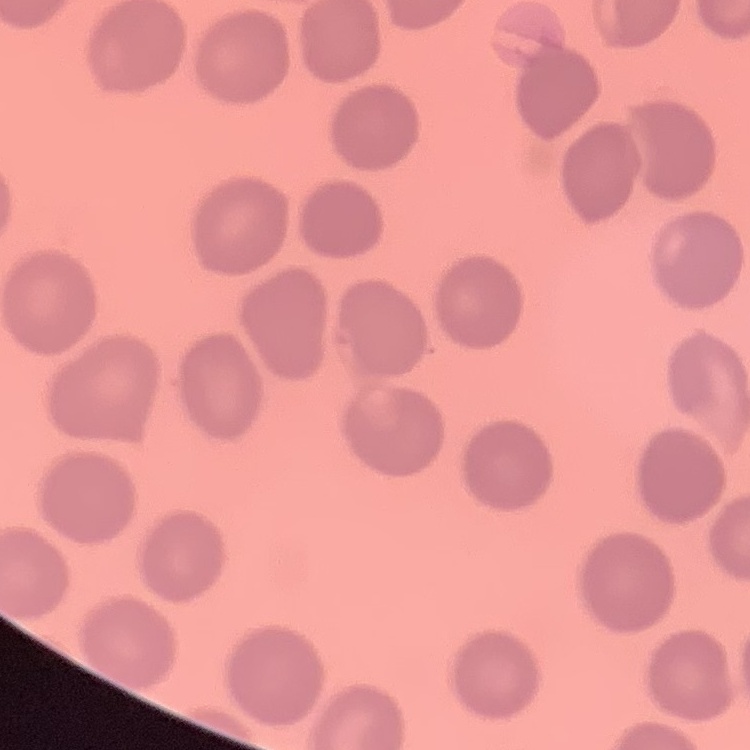

The erythrocytes exhibit no rouleaux formation. Stained with either Field's or Giemsa. Thin peripheral smear. One tile cut from a larger photomicrograph.